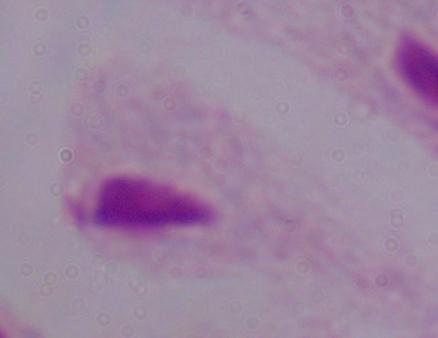

Summary:
  - Magnification: 1000x
  - Identification: trichomonad
  - Modality: photomicrograph